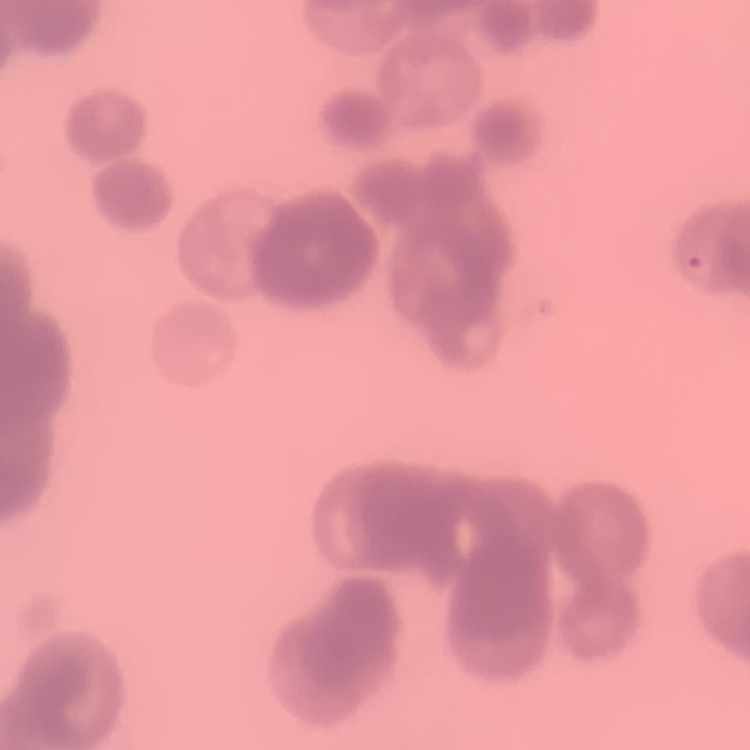

erythrocyte morphology = rouleaux formation
image type = square crop of a larger photomicrograph
stain = Field's or Giemsa
preparation = thin blood smear